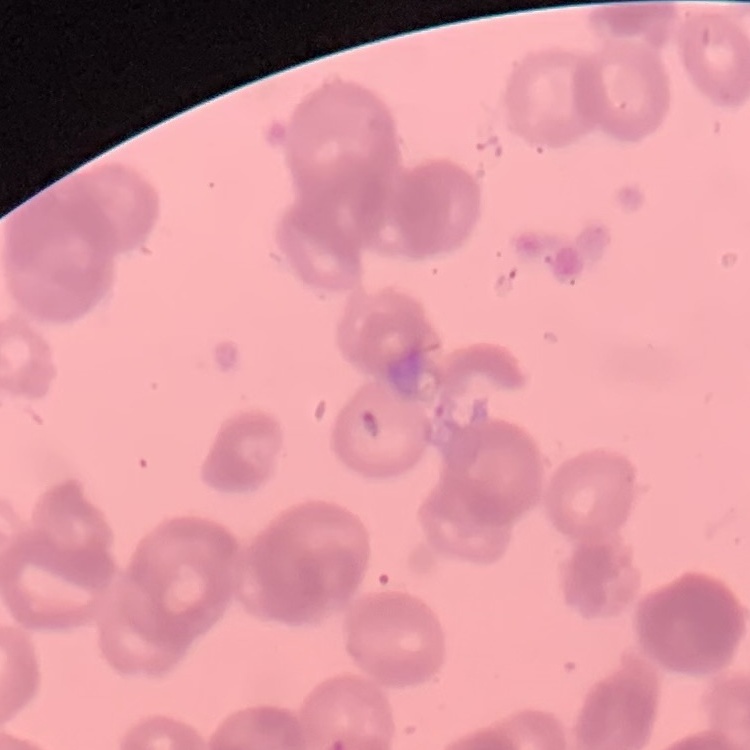

Summary:
  - Erythrocyte morphology: rouleaux formation
  - Image type: square crop of a larger photomicrograph
  - Preparation: thin peripheral smear
  - Stain: Field's or Giemsa